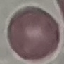
result: no malaria parasites seen
image_type: automatically extracted cell patch, resized to 64 × 64 pixels
capture: smartphone through the microscope eyepiece
preparation: thin smear
stain: Giemsa